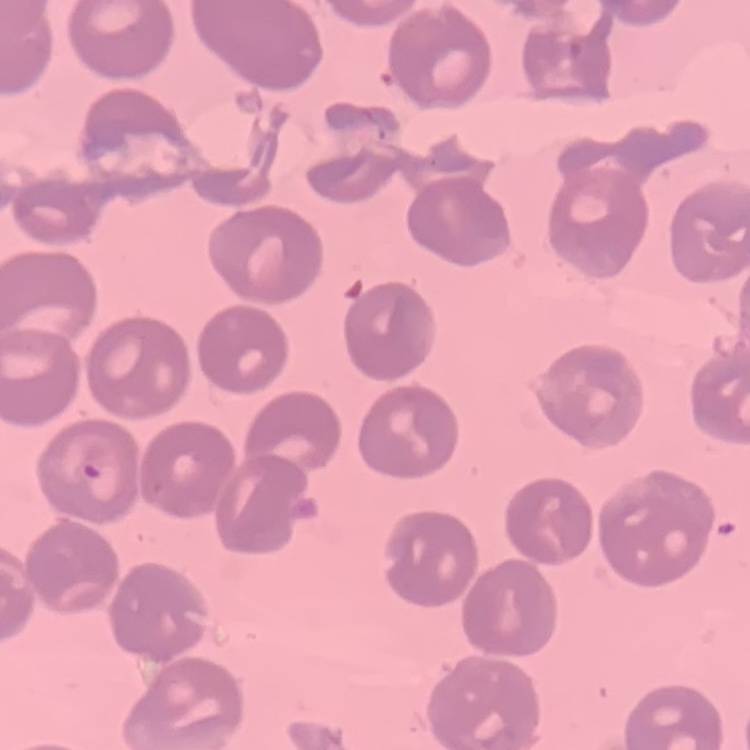

Summary:
  - Red blood cell morphology: no rouleaux formation
  - Preparation: thin blood film
  - Image type: one tile cut from a larger photomicrograph
  - Stain: Field's or Giemsa